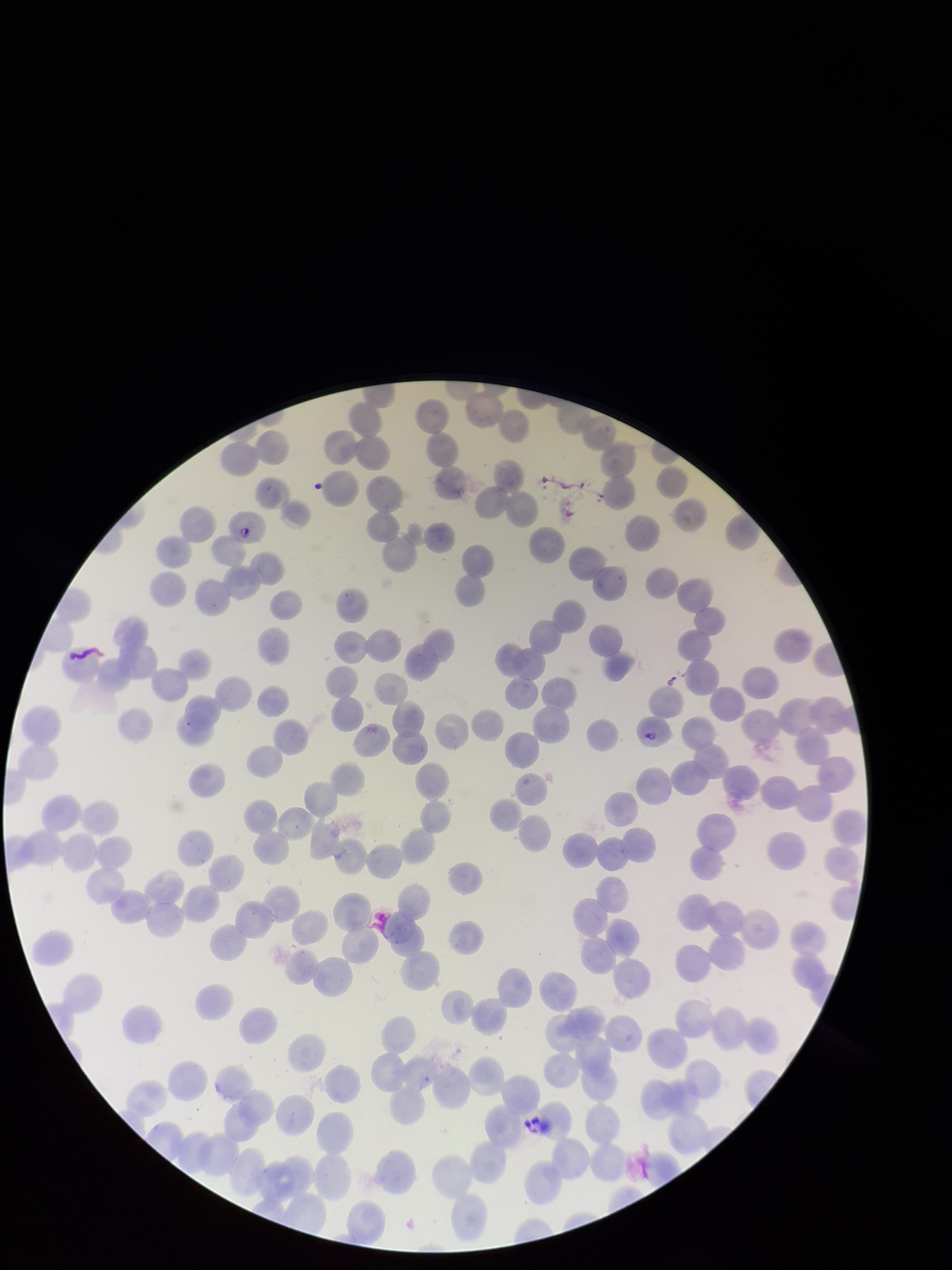

Patient malaria status: positive. Giemsa stain. Preparation: thin smear. Species reported for this patient: Plasmodium falciparum. Red blood cell count: 201. Photographed through the microscope eyepiece with a smartphone camera. Parasitized red blood cell count: 2. Parasitized red blood cells: detected. Image is 952×1270 pixels. Single field of view.